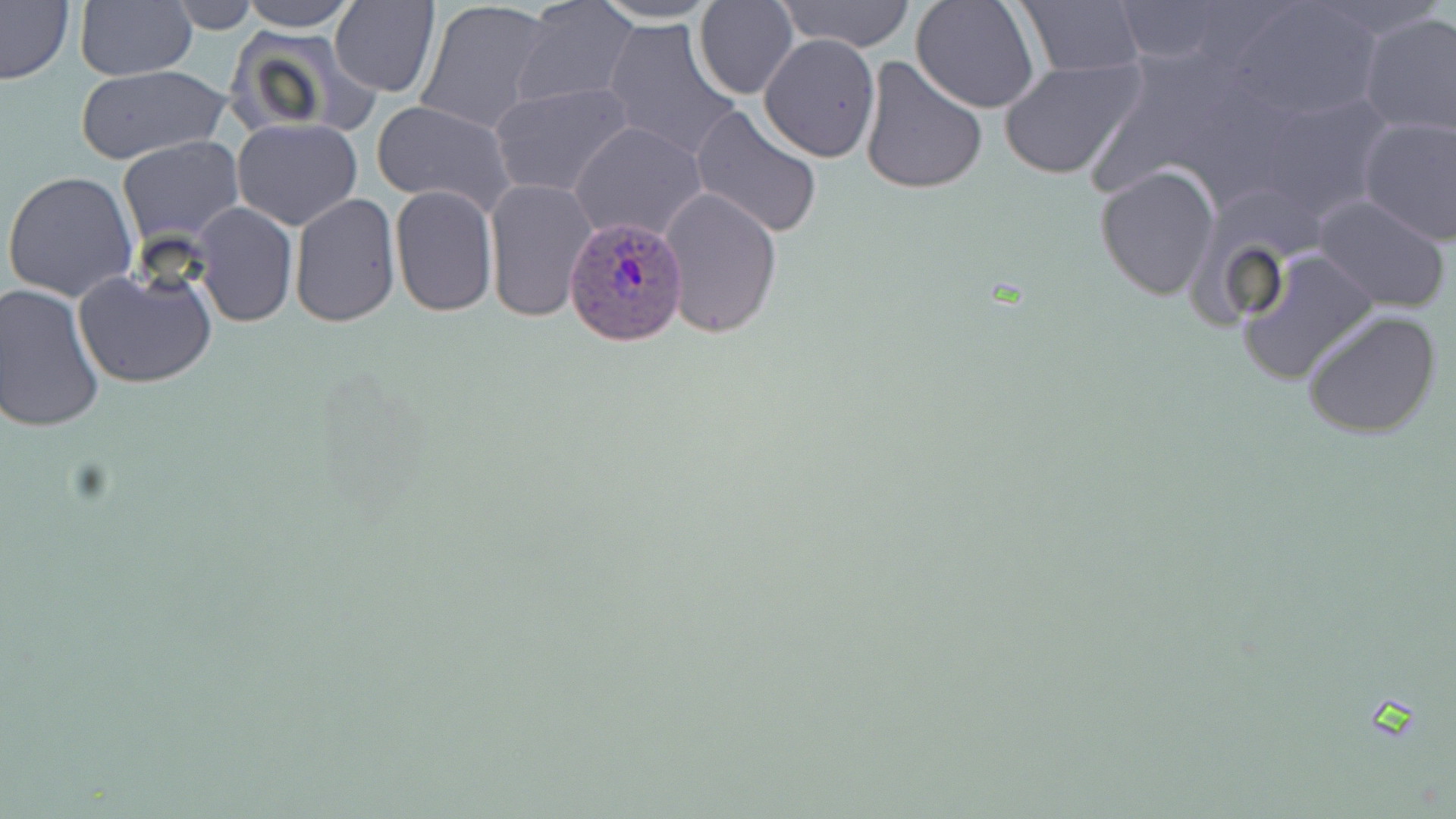

Summary:
  - Coordinate format: approximate bounding boxes as [x1, y1, x2, y2] in pixels
  - Plasmodium ovale-infected red blood cell locations: [567, 214, 691, 348]
  - Uninfected red blood cell locations: [0, 0, 75, 87], [75, 0, 196, 80], [165, 0, 260, 32], [239, 0, 358, 31], [592, 0, 722, 24], [694, 0, 799, 100], [776, 0, 917, 51], [512, 1, 637, 107], [910, 1, 1039, 113], [1223, 1, 1384, 124], [330, 2, 439, 96], [415, 2, 555, 136], [1016, 2, 1146, 78], [1103, 3, 1262, 69], [1356, 10, 1456, 141], [601, 18, 740, 159], [225, 28, 374, 143], [759, 34, 880, 163], [858, 54, 988, 196], [997, 58, 1146, 181], [76, 65, 229, 165], [491, 82, 633, 199], [1237, 84, 1399, 220], [371, 98, 517, 214], [689, 105, 825, 238], [1358, 114, 1456, 245], [231, 118, 363, 230], [572, 121, 707, 242], [117, 137, 242, 249], [1094, 164, 1221, 300], [3, 171, 138, 303], [483, 178, 599, 325], [389, 185, 497, 317], [658, 185, 783, 339], [1312, 192, 1455, 314], [289, 193, 401, 327], [193, 202, 297, 327], [1236, 246, 1381, 387], [72, 263, 218, 389], [0, 284, 105, 432], [1299, 307, 1444, 441]
  - Slide-level diagnosis: Plasmodium ovale
  - Field of view: one of a larger specimen
  - Image size: 1456×819 pixels
  - Preparation: thin blood smear
  - Stain: May-Grünwald-Giemsa
  - Magnification: 1000x
  - Modality: light microscopy